Identify the blood parasite species.
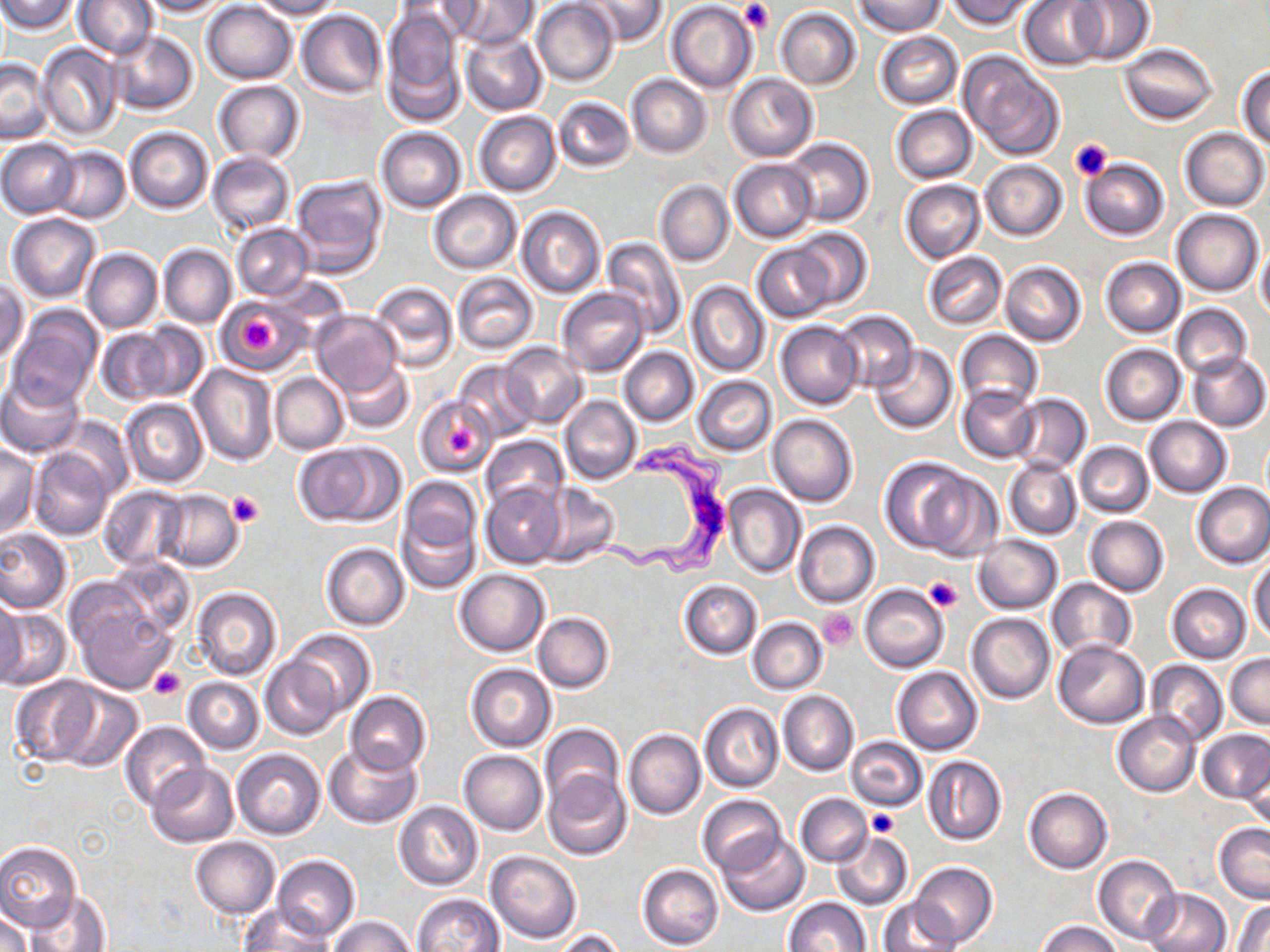
Trypanosoma brucei.

stain: May-Grünwald-Giemsa
preparation: thin blood smear
modality: optical microscopy
trypanosoma_brucei_locations: 'approximate bounding boxes as [x1, y1, x2, y2] in pixels: [590, 437, 729, 574]'
magnification: 1000x
image_size: 1270×952 pixels
field_of_view: one of a larger specimen
platelet_locations: 'approximate bounding boxes as [x1, y1, x2, y2] in pixels: [741, 0, 773, 31], [1068, 137, 1113, 181], [241, 317, 278, 350], [446, 424, 480, 463], [227, 490, 262, 529], [922, 576, 962, 613], [817, 609, 859, 650], [149, 669, 185, 699], [869, 809, 899, 838]'
uninfected_red_blood_cell_locations: 'approximate bounding boxes as [x1, y1, x2, y2] in pixels: [74, 0, 156, 58], [137, 0, 231, 16], [250, 0, 343, 20], [446, 0, 536, 47], [575, 0, 667, 45], [854, 0, 946, 37], [1021, 0, 1110, 70], [1068, 0, 1155, 65], [1, 1, 78, 33], [532, 1, 619, 86], [666, 1, 756, 92], [946, 1, 1037, 29], [201, 2, 297, 83], [381, 7, 467, 127], [775, 7, 862, 90], [295, 9, 386, 99], [107, 30, 198, 116], [459, 31, 546, 116], [874, 31, 962, 109], [37, 43, 122, 140], [1119, 43, 1216, 126], [959, 54, 1065, 162], [0, 59, 51, 143], [1237, 65, 1270, 149], [627, 74, 712, 158], [726, 75, 817, 161], [213, 80, 305, 163], [553, 96, 633, 171], [892, 106, 976, 183], [473, 111, 561, 197], [123, 126, 214, 213], [376, 127, 467, 212], [1180, 127, 1269, 211], [0, 138, 80, 217], [784, 138, 874, 226], [51, 147, 131, 223], [207, 152, 295, 234], [729, 158, 818, 242], [1079, 158, 1168, 241], [981, 160, 1067, 240], [289, 174, 388, 276], [901, 179, 985, 263], [654, 180, 733, 267], [428, 190, 521, 273], [515, 205, 605, 299], [1172, 208, 1264, 296], [7, 213, 102, 304], [232, 223, 314, 300], [790, 226, 873, 310], [601, 236, 687, 339], [752, 243, 835, 323], [158, 244, 237, 329], [1256, 244, 1270, 322], [80, 247, 163, 334], [921, 252, 1006, 330], [1101, 257, 1186, 338], [1000, 261, 1086, 346], [452, 271, 540, 356], [265, 274, 352, 333], [1, 280, 27, 367], [370, 280, 458, 373], [687, 281, 769, 376], [557, 288, 648, 375], [217, 300, 296, 373], [1172, 304, 1251, 379], [7, 306, 102, 410], [310, 310, 402, 395], [834, 310, 918, 390], [132, 320, 210, 404], [776, 320, 863, 409], [95, 328, 172, 406], [956, 329, 1042, 412], [871, 343, 958, 434], [500, 344, 588, 427], [1099, 344, 1186, 425], [618, 347, 699, 425], [1187, 350, 1269, 431], [453, 360, 538, 441], [337, 361, 416, 433], [188, 364, 279, 468], [271, 372, 349, 454], [1, 375, 84, 458], [693, 376, 776, 456], [957, 384, 1038, 463], [1011, 394, 1091, 474], [560, 395, 641, 486], [417, 396, 498, 475], [120, 397, 208, 487], [768, 414, 858, 507], [1143, 416, 1231, 497], [53, 417, 134, 500], [481, 435, 567, 513], [1075, 441, 1153, 517], [0, 442, 40, 536], [293, 442, 400, 527], [28, 447, 117, 541], [880, 458, 977, 554], [1005, 459, 1082, 538], [915, 469, 1003, 560], [395, 476, 482, 589], [536, 482, 619, 568], [1192, 482, 1270, 568], [481, 483, 565, 567], [99, 485, 191, 571], [723, 485, 805, 579], [156, 491, 243, 572], [1084, 515, 1169, 595], [793, 521, 880, 608], [0, 529, 71, 614], [973, 535, 1061, 613], [321, 542, 409, 630], [107, 557, 197, 641], [1249, 559, 1269, 645], [454, 568, 550, 656], [1046, 578, 1136, 660], [678, 579, 761, 659], [67, 584, 177, 693], [860, 584, 948, 673], [1168, 584, 1251, 663], [192, 588, 282, 679], [0, 597, 26, 687], [0, 607, 71, 691], [534, 612, 615, 693], [966, 613, 1055, 703], [748, 618, 827, 693], [284, 630, 374, 717], [1053, 639, 1149, 728], [1225, 653, 1269, 729], [261, 657, 342, 739], [1147, 660, 1226, 746], [466, 663, 556, 752], [893, 666, 982, 755], [9, 676, 102, 767], [184, 677, 263, 754], [50, 688, 144, 774], [779, 690, 859, 776], [345, 691, 431, 775], [700, 703, 783, 792], [1112, 711, 1199, 796], [119, 720, 209, 810], [539, 722, 624, 814], [624, 728, 705, 820], [1198, 731, 1270, 802], [847, 738, 925, 810], [324, 742, 422, 828], [232, 748, 326, 840], [458, 750, 547, 834], [1243, 754, 1269, 837], [923, 755, 1005, 846], [147, 763, 238, 847], [543, 769, 633, 861], [1023, 787, 1113, 873], [795, 792, 872, 866], [697, 794, 784, 875], [394, 802, 483, 890], [1214, 823, 1270, 903], [831, 831, 913, 910], [717, 832, 810, 916], [188, 837, 280, 917], [0, 842, 81, 931], [485, 849, 582, 945], [1092, 854, 1182, 947], [273, 855, 360, 942], [909, 861, 997, 949], [637, 864, 723, 951], [1142, 888, 1231, 952], [2, 889, 49, 950], [24, 889, 115, 951], [413, 892, 503, 952], [784, 897, 870, 952], [878, 898, 957, 952], [1232, 899, 1269, 952], [239, 906, 333, 951], [1, 907, 31, 952], [327, 915, 418, 952], [1037, 920, 1121, 952], [554, 928, 627, 952]'